Assess this cell for malaria.
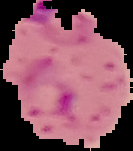
It is parasitized.

From a thin blood film. Image is 133×151 pixels. The area outside the segmented cell region is set to black.